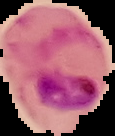

preparation = thin blood smear
image type = segmented cell region on a black background
malaria status = parasitized
image size = 115×136 pixels